Give the preparation type.
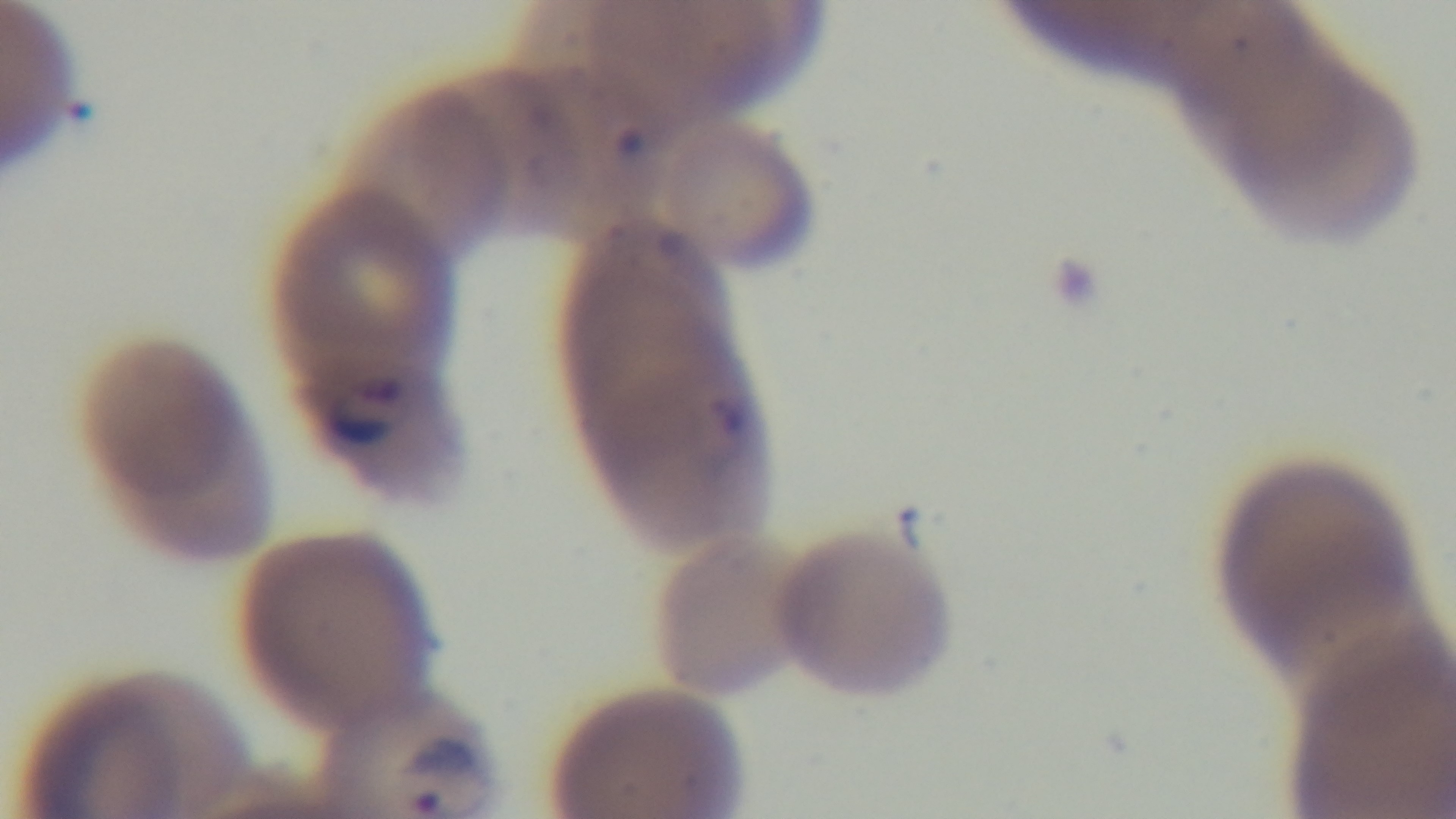
A thin smear.

Light microscopy. 100x oil-immersion objective. Single field of view. Malaria status: positive. Mounted 4K digital camera. Giemsa-stained.